Comment on the morphology of the red blood cells.
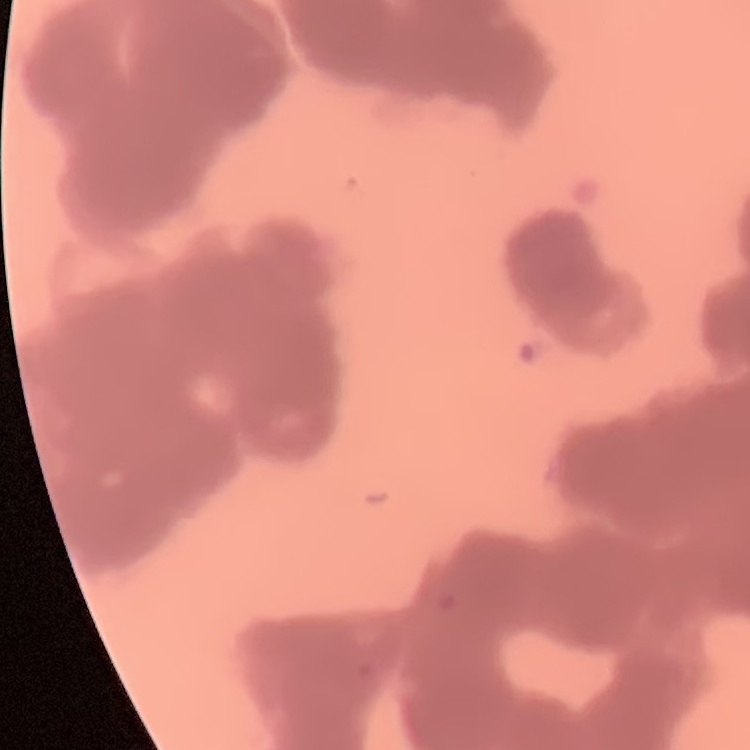

Rouleaux formation.

stain = Field's or Giemsa
preparation = thin blood smear
image type = square crop of a larger photomicrograph